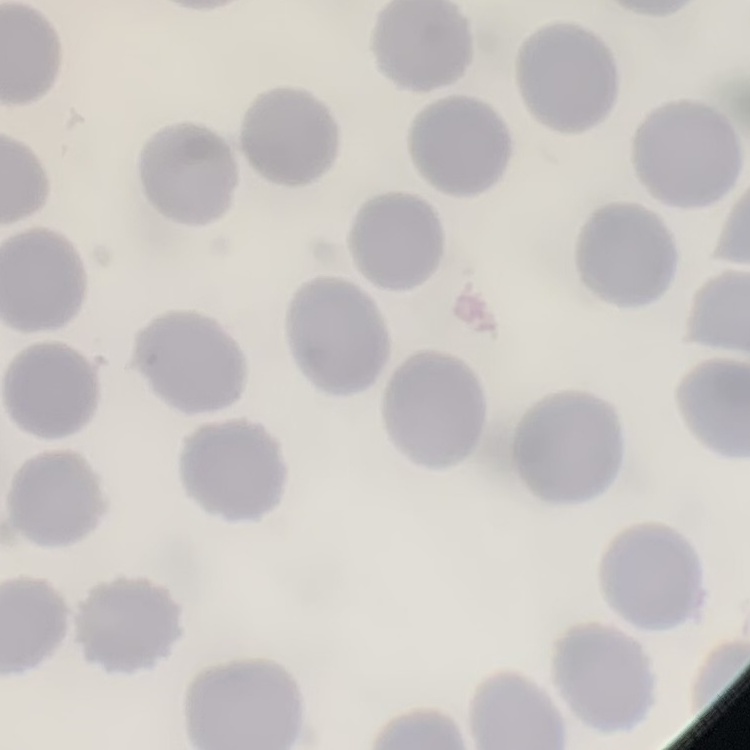

red_blood_cell_morphology: no rouleaux formation
image_type: square crop of a larger photomicrograph
stain: Field's or Giemsa
preparation: thin peripheral smear